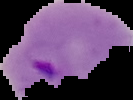 From a thin blood film. Malaria status: parasitized. Image is 133×100 pixels. Cell region segmented out of the field of view; the surrounding area is masked to black.